Report the malaria status of this cell.
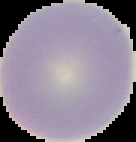
It is uninfected.

Cell region segmented out of the field of view; the surrounding area is masked to black. Image is 136×142 pixels. From a thin blood smear.